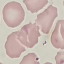
result = no malaria parasites seen
stain = Giemsa
image type = automatically extracted cell patch, resized to 64 × 64 pixels
preparation = thin blood film
capture = smartphone camera at the microscope eyepiece